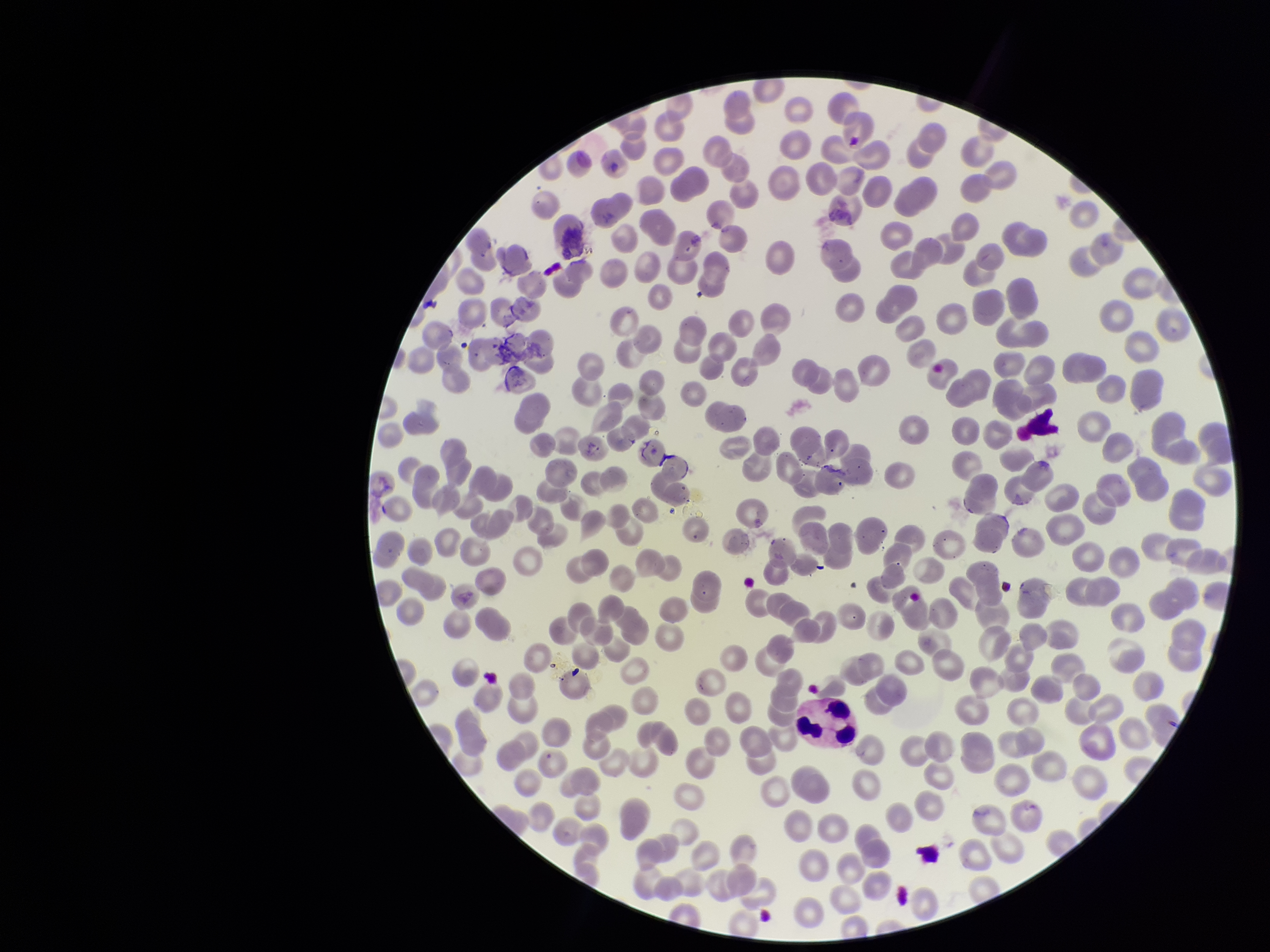

Patient malaria status: negative. Parasitized red blood cells: none identified. One field from this slide. Stained with Giemsa. Red blood cell count: 272. Parasitized red blood cell count: 0. Preparation: thin. Image is 1270×952 pixels. Photographed through the microscope eyepiece with a smartphone camera.